Assess for malaria.
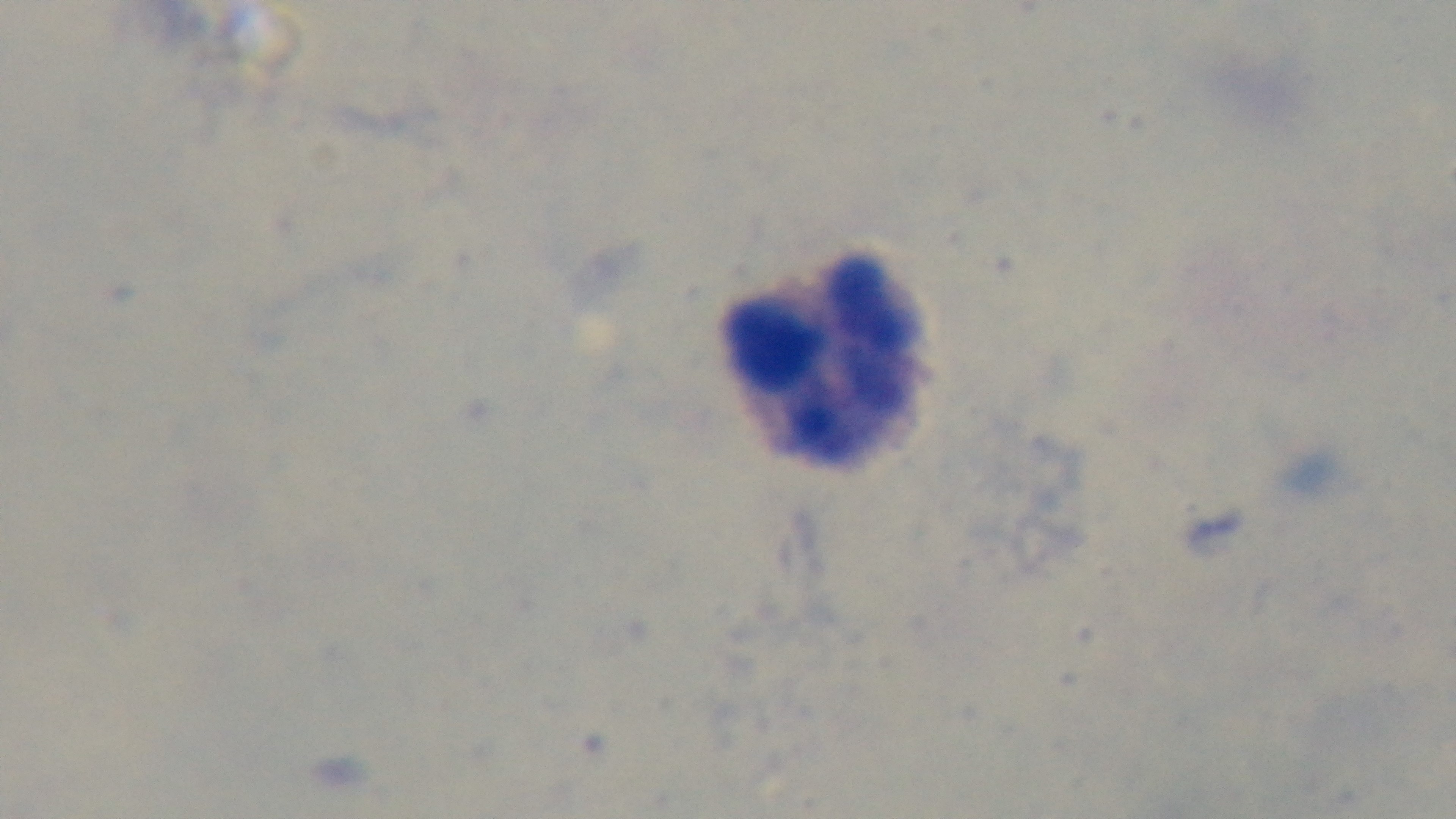
Negative.

Summary:
  - Capture: mounted 4K digital camera
  - Stain: Giemsa
  - Objective: 100x oil immersion
  - Field of view: one from the slide
  - Modality: light microscopy
  - Preparation: thick